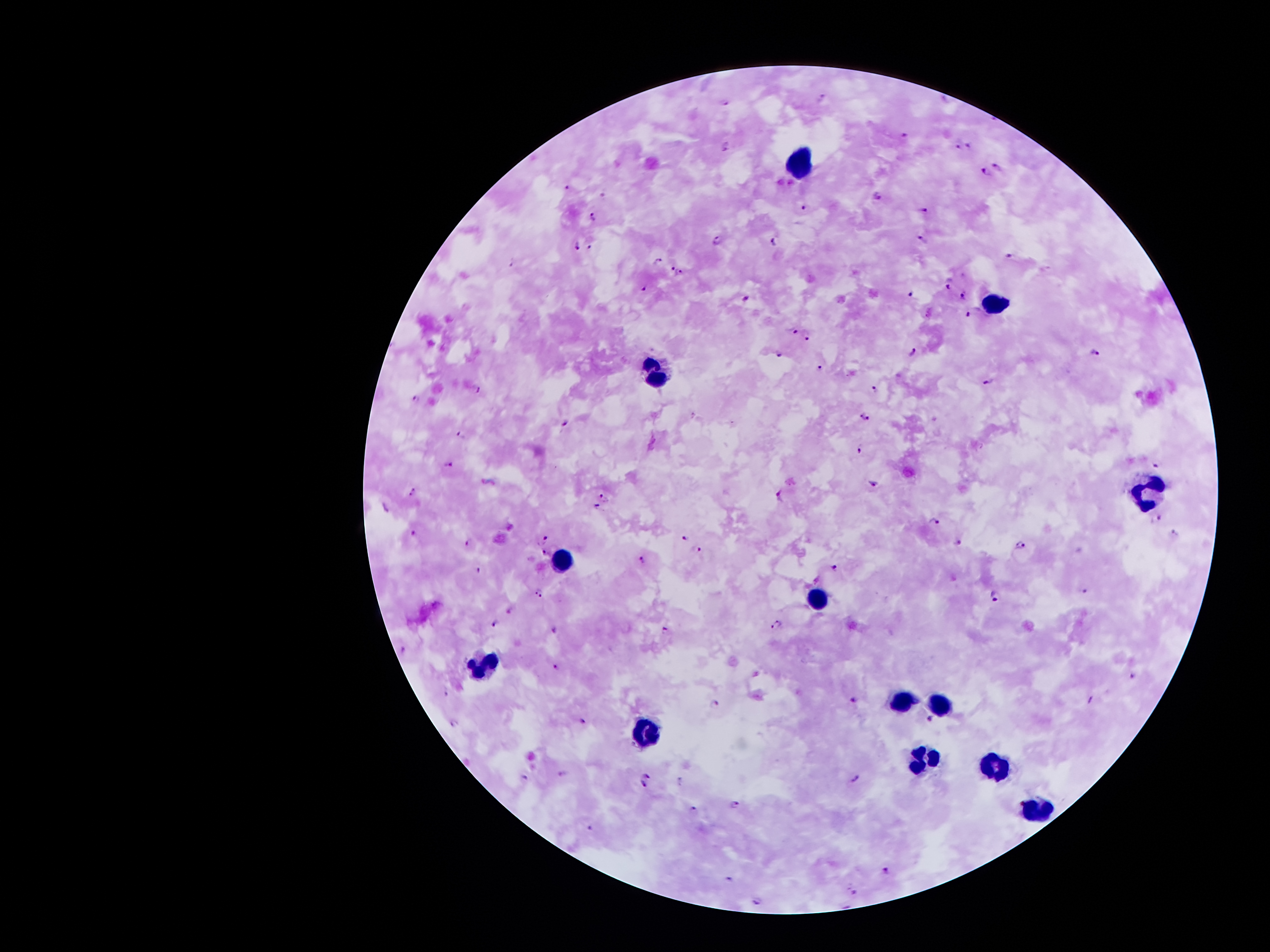
Approximate centers as {x, y} in pixels.
Summary:
  - Plasmodium parasite locations: {823, 96}, {726, 103}, {903, 135}, {726, 145}, {959, 146}, {969, 146}, {999, 166}, {985, 173}, {568, 186}, {878, 196}, {804, 207}, {924, 209}, {593, 216}, {921, 238}, {718, 241}, {775, 241}, {590, 244}, {577, 246}, {1010, 255}, {657, 260}, {670, 265}, {679, 273}, {947, 283}, {643, 288}, {911, 293}, {964, 294}, {747, 298}, {969, 314}, {792, 331}, {808, 336}, {911, 349}, {781, 353}, {1096, 353}, {820, 368}, {988, 383}, {477, 389}, {875, 390}, {415, 396}, {865, 415}, {564, 424}, {462, 434}, {860, 448}, {1156, 464}, {450, 465}, {874, 482}, {413, 493}, {604, 495}, {780, 496}, {598, 505}, {386, 508}, {1157, 519}, {934, 522}, {414, 532}, {1174, 534}, {684, 535}, {545, 538}, {468, 541}, {958, 542}, {1021, 546}, {699, 550}, {546, 555}, {643, 559}, {833, 566}, {479, 569}, {1085, 588}, {538, 593}, {995, 596}, {510, 608}, {494, 624}, {777, 624}, {554, 630}, {665, 630}, {405, 654}, {556, 667}, {1135, 673}, {447, 692}, {1091, 699}, {853, 701}, {715, 705}, {929, 719}, {581, 722}, {455, 723}, {647, 775}, {856, 776}, {526, 779}, {680, 781}, {644, 788}, {734, 804}, {693, 807}, {591, 827}, {888, 870}, {729, 879}, {856, 892}, {757, 901}
  - Leukocyte locations: {797, 164}, {996, 298}, {654, 370}, {1149, 488}, {561, 559}, {817, 597}, {481, 664}, {904, 696}, {935, 698}, {644, 732}, {922, 759}, {994, 765}, {1039, 813}
  - Stain: Giemsa
  - Capture: smartphone through the microscope eyepiece
  - Field of view: single
  - Image size: 1270×952 pixels
  - Magnification: 100x
  - Preparation: thick peripheral-blood smear
  - Patient malaria status: positive for Plasmodium falciparum